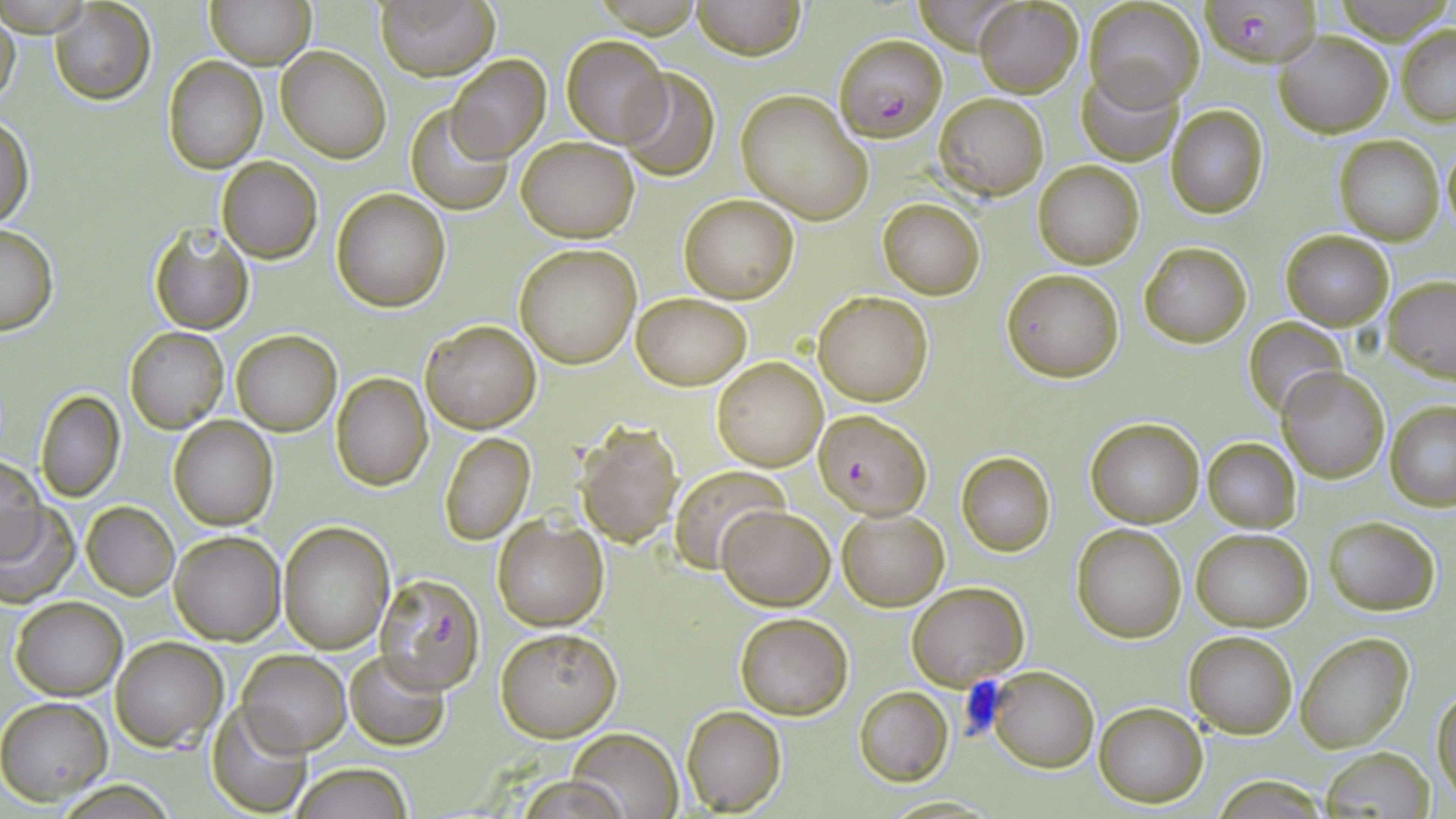 Approximate bounding boxes as named x1/y1/x2/y2 corners in pixels. Uninfected red blood cell locations: (x1=209, y1=0, x2=315, y2=69), (x1=373, y1=0, x2=499, y2=79), (x1=692, y1=0, x2=805, y2=59), (x1=1085, y1=0, x2=1205, y2=109), (x1=1333, y1=0, x2=1448, y2=42), (x1=48, y1=1, x2=156, y2=105), (x1=913, y1=1, x2=1018, y2=52), (x1=972, y1=2, x2=1083, y2=96), (x1=0, y1=10, x2=21, y2=115), (x1=1397, y1=23, x2=1456, y2=124), (x1=1276, y1=31, x2=1393, y2=136), (x1=560, y1=34, x2=670, y2=146), (x1=276, y1=47, x2=390, y2=163), (x1=444, y1=55, x2=551, y2=162), (x1=163, y1=56, x2=267, y2=173), (x1=617, y1=67, x2=722, y2=182), (x1=1079, y1=68, x2=1180, y2=164), (x1=736, y1=91, x2=872, y2=223), (x1=935, y1=92, x2=1048, y2=198), (x1=406, y1=104, x2=513, y2=216), (x1=1166, y1=104, x2=1270, y2=218), (x1=0, y1=113, x2=34, y2=232), (x1=1335, y1=134, x2=1444, y2=245), (x1=516, y1=136, x2=639, y2=241), (x1=1440, y1=141, x2=1456, y2=237), (x1=217, y1=157, x2=323, y2=263), (x1=1033, y1=160, x2=1145, y2=268), (x1=332, y1=189, x2=452, y2=311), (x1=679, y1=194, x2=799, y2=303), (x1=878, y1=199, x2=985, y2=299), (x1=0, y1=222, x2=59, y2=335), (x1=148, y1=223, x2=255, y2=335), (x1=1281, y1=231, x2=1392, y2=330), (x1=1138, y1=241, x2=1252, y2=348), (x1=514, y1=243, x2=642, y2=369), (x1=1001, y1=268, x2=1124, y2=382), (x1=1383, y1=277, x2=1456, y2=382), (x1=632, y1=291, x2=752, y2=389), (x1=813, y1=291, x2=934, y2=405), (x1=1244, y1=317, x2=1350, y2=420), (x1=421, y1=320, x2=541, y2=434), (x1=124, y1=326, x2=229, y2=433), (x1=231, y1=329, x2=341, y2=436), (x1=712, y1=356, x2=829, y2=471), (x1=1278, y1=368, x2=1391, y2=482), (x1=332, y1=372, x2=432, y2=490), (x1=34, y1=389, x2=126, y2=503), (x1=1386, y1=401, x2=1456, y2=510), (x1=168, y1=416, x2=277, y2=530), (x1=1086, y1=419, x2=1204, y2=527), (x1=576, y1=423, x2=683, y2=545), (x1=438, y1=431, x2=536, y2=545), (x1=1203, y1=438, x2=1300, y2=532), (x1=955, y1=452, x2=1055, y2=556), (x1=1, y1=453, x2=46, y2=562), (x1=671, y1=469, x2=789, y2=570), (x1=82, y1=501, x2=180, y2=600), (x1=0, y1=505, x2=76, y2=605), (x1=717, y1=506, x2=833, y2=610), (x1=838, y1=509, x2=949, y2=609), (x1=1323, y1=515, x2=1441, y2=615), (x1=493, y1=517, x2=607, y2=630), (x1=277, y1=521, x2=394, y2=653), (x1=1072, y1=524, x2=1186, y2=642), (x1=1192, y1=528, x2=1311, y2=631), (x1=169, y1=530, x2=285, y2=644), (x1=907, y1=581, x2=1029, y2=687), (x1=11, y1=597, x2=126, y2=700), (x1=735, y1=613, x2=853, y2=718), (x1=495, y1=627, x2=621, y2=740), (x1=1184, y1=631, x2=1297, y2=739), (x1=1297, y1=633, x2=1412, y2=752), (x1=111, y1=637, x2=227, y2=752), (x1=343, y1=649, x2=450, y2=749), (x1=239, y1=651, x2=352, y2=754), (x1=984, y1=668, x2=1098, y2=773), (x1=1432, y1=686, x2=1456, y2=805), (x1=854, y1=687, x2=954, y2=785), (x1=0, y1=696, x2=113, y2=804), (x1=207, y1=700, x2=312, y2=816), (x1=1094, y1=701, x2=1208, y2=806), (x1=681, y1=706, x2=785, y2=814), (x1=568, y1=728, x2=683, y2=818), (x1=1319, y1=747, x2=1434, y2=818), (x1=290, y1=764, x2=413, y2=819), (x1=508, y1=774, x2=634, y2=819). Plasmodium falciparum-infected red blood cell locations: (x1=1200, y1=1, x2=1321, y2=64), (x1=835, y1=34, x2=948, y2=140), (x1=813, y1=409, x2=931, y2=519), (x1=373, y1=568, x2=484, y2=694). Slide-level diagnosis: Plasmodium falciparum. Optical microscopy. Thin blood smear. Image is 1456×819 pixels. May-Grünwald-Giemsa stain. Single field of view. 1000x magnification.